Assess this cell for malaria.
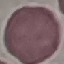
Uninfected.

Thin smear of blood. Acquired by smartphone through the microscope eyepiece. Giemsa stain. Cell patch, automatically extracted from a larger field of view and resized to 64 × 64 pixels.